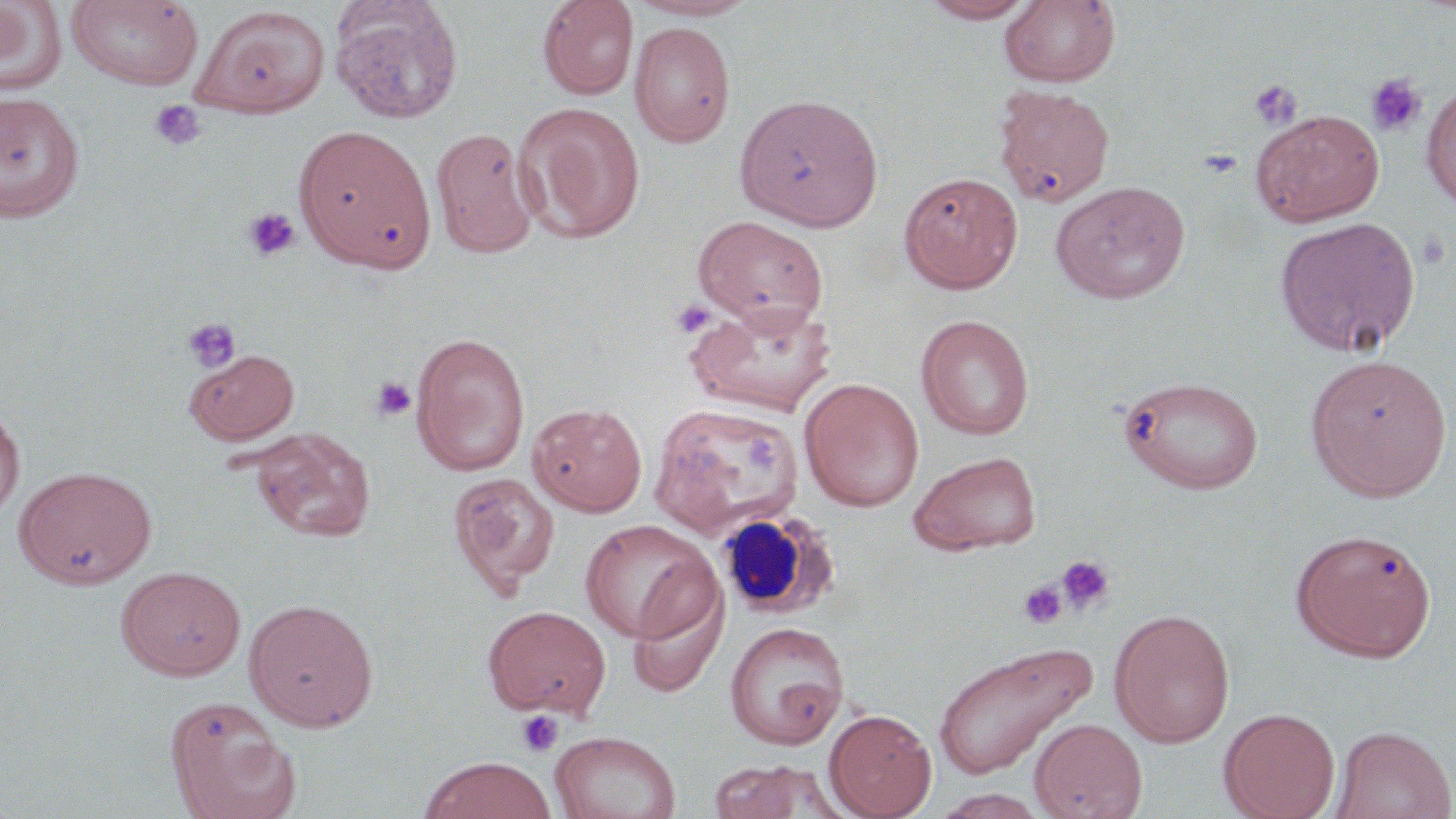

Summary:
  - Coordinate format: approximate bounding boxes as (x1,y1)-(x2,y2) corner pairs in pixels
  - Platelet locations: (1364,73)-(1428,138), (1248,79)-(1302,130), (149,100)-(206,151), (1198,148)-(1243,179), (243,207)-(301,262), (1416,228)-(1452,271), (671,299)-(715,338), (181,317)-(242,374), (369,377)-(416,422), (1057,556)-(1114,615), (1020,581)-(1067,629), (516,710)-(564,757)
  - Uninfected red blood cell locations: (0,0)-(67,97), (66,0)-(204,90), (330,0)-(464,124), (537,0)-(638,100), (625,0)-(759,21), (920,0)-(1040,23), (1000,1)-(1121,88), (192,6)-(330,118), (629,22)-(736,146), (1421,82)-(1456,212), (993,85)-(1115,208), (0,92)-(85,223), (734,93)-(884,231), (512,102)-(646,244), (1251,109)-(1385,227), (294,124)-(435,273), (431,127)-(539,258), (898,170)-(1023,293), (1050,180)-(1192,304), (693,216)-(828,332), (1274,216)-(1421,358), (685,300)-(837,417), (916,314)-(1034,440), (411,332)-(530,476), (184,348)-(299,445), (1305,353)-(1452,501), (1119,374)-(1265,495), (799,377)-(924,512), (528,402)-(647,516), (649,402)-(803,539), (0,405)-(24,525), (250,427)-(375,542), (909,450)-(1041,556), (15,466)-(157,588), (446,471)-(560,597), (579,518)-(719,644), (1291,528)-(1436,662), (116,565)-(246,681), (626,576)-(729,697), (244,598)-(378,731), (482,605)-(611,718), (1109,608)-(1235,747), (724,622)-(849,749), (931,639)-(1097,780), (165,696)-(298,817), (1218,707)-(1341,819), (824,708)-(936,819), (1029,718)-(1147,819), (1330,725)-(1455,819), (550,730)-(681,819), (420,756)-(555,818), (707,759)-(845,818)
  - White blood cell locations: (713,508)-(841,620)
  - Slide-level diagnosis: no evidence of blood parasites
  - Stain: May-Grünwald-Giemsa
  - Preparation: thin blood smear
  - Image size: 1456×819 pixels
  - Magnification: 1000x
  - Modality: light microscopy
  - Field of view: one of a larger specimen